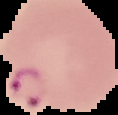
malaria_status: parasitized
image_size: 118×115 pixels
image_type: segmented cell region with the area outside set to black
preparation: thin blood film